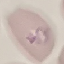

Summary:
  - Result: malaria parasites detected
  - Capture: smartphone through the microscope eyepiece
  - Stain: Giemsa
  - Preparation: thin blood film
  - Image type: cell patch, automatically extracted from a larger field of view and resized to 64 × 64 pixels